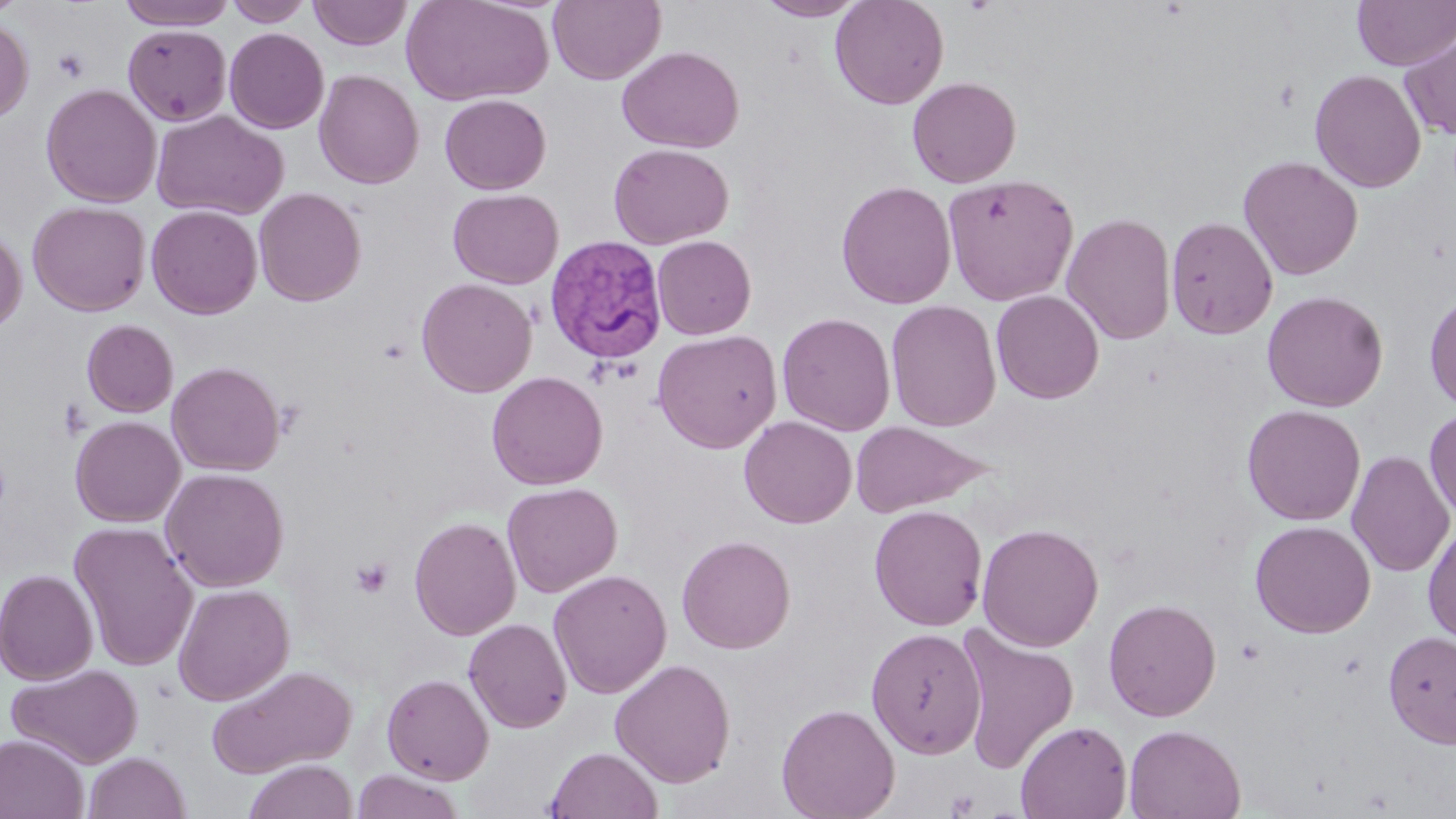 Approximate bounding boxes as [x1, y1, x2, y2] in pixels. Platelet locations: [52, 48, 90, 83], [350, 557, 393, 599], [946, 789, 980, 817]. Plasmodium vivax-infected red blood cell locations: [550, 236, 673, 363]. Uninfected red blood cell locations: [119, 0, 237, 29], [224, 0, 313, 26], [401, 0, 554, 106], [548, 0, 665, 85], [754, 0, 866, 21], [830, 0, 949, 110], [1352, 0, 1456, 70], [307, 1, 412, 50], [0, 17, 34, 123], [122, 24, 232, 126], [224, 27, 329, 134], [1399, 27, 1456, 140], [617, 46, 744, 153], [1310, 68, 1427, 193], [314, 70, 424, 189], [906, 76, 1021, 188], [41, 83, 161, 208], [439, 94, 552, 195], [151, 109, 288, 221], [608, 142, 734, 249], [1238, 155, 1363, 280], [940, 172, 1079, 306], [836, 180, 957, 309], [254, 188, 366, 307], [447, 188, 564, 289], [27, 200, 150, 316], [146, 205, 263, 319], [1061, 212, 1177, 345], [1165, 216, 1278, 339], [0, 225, 27, 334], [651, 235, 757, 340], [416, 278, 537, 397], [991, 290, 1104, 404], [1261, 290, 1388, 412], [1424, 290, 1456, 413], [886, 300, 1002, 433], [777, 312, 896, 436], [81, 319, 178, 417], [652, 329, 783, 453], [167, 361, 286, 476], [487, 371, 608, 490], [1242, 404, 1365, 525], [1424, 407, 1456, 523], [70, 415, 185, 527], [738, 416, 857, 528], [849, 420, 989, 518], [1346, 450, 1454, 577], [161, 467, 289, 592], [502, 482, 622, 597], [869, 504, 988, 631], [409, 515, 521, 640], [1250, 519, 1376, 638], [68, 521, 198, 671], [1423, 521, 1456, 645], [976, 522, 1104, 651], [676, 534, 795, 654], [0, 568, 99, 685], [549, 569, 672, 698], [173, 583, 294, 705], [1103, 598, 1222, 721], [463, 617, 572, 733], [954, 624, 1079, 773], [866, 627, 986, 758], [1383, 630, 1456, 748], [610, 658, 736, 787], [7, 662, 143, 768], [205, 665, 358, 778], [381, 672, 494, 784], [776, 702, 901, 819], [1015, 719, 1133, 819], [1124, 724, 1246, 818], [0, 734, 89, 819], [545, 746, 663, 819], [83, 751, 192, 819], [244, 758, 358, 819], [350, 770, 466, 819]. Slide-level diagnosis: Plasmodium vivax. One field of a larger specimen. Thin blood smear. May-Grünwald-Giemsa-stained preparation. Light microscopy. Image is 1456×819 pixels. Captured at 1000x magnification.